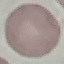
Summary:
  - Malaria status: uninfected
  - Image type: cell patch, automatically extracted from a larger field of view and resized to 64 × 64 pixels
  - Stain: Giemsa
  - Preparation: thin blood smear
  - Capture: smartphone through the microscope eyepiece